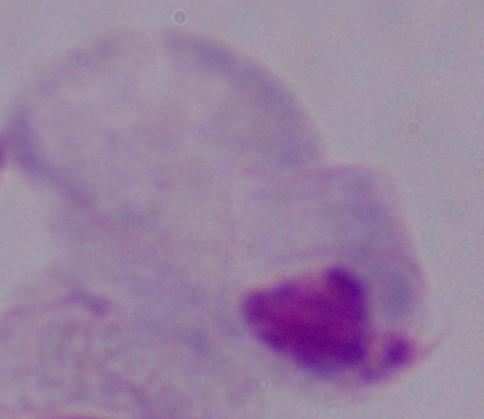

A trichomonad is seen. 1000x magnification. Micrograph.